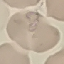
result = negative for malaria parasites
stain = Giemsa
capture = smartphone camera at the microscope eyepiece
preparation = thin blood smear
image type = cell patch, automatically extracted from a larger field of view and resized to 64 × 64 pixels